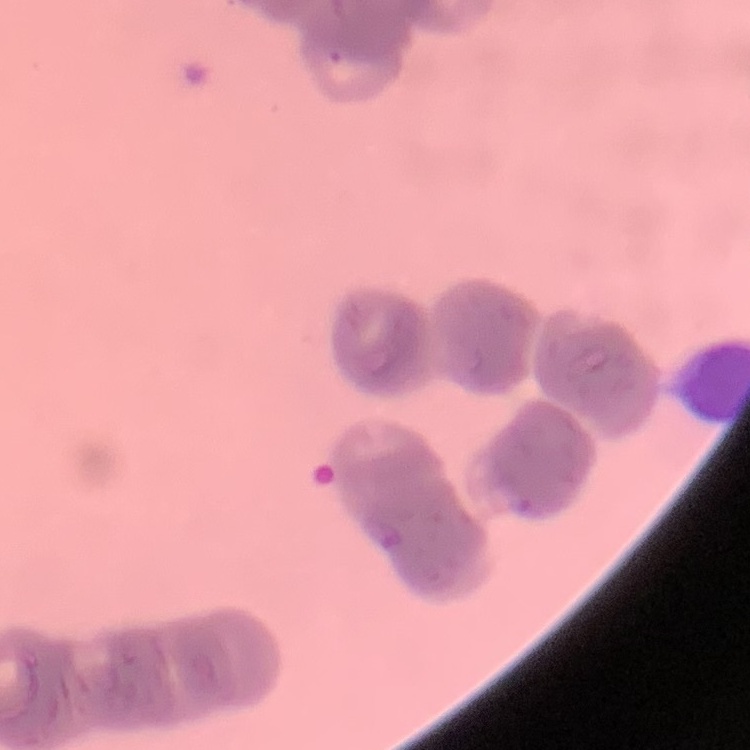
The erythrocytes show rouleaux formation. Thin blood film. Stained with either Field's or Giemsa. One tile cut from a larger photomicrograph.